Assess this cell for malaria.
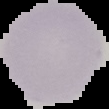
Uninfected.

Segmented cell region on a black background. Image is 109×109 pixels. From a thin blood film.